Evaluate for malaria.
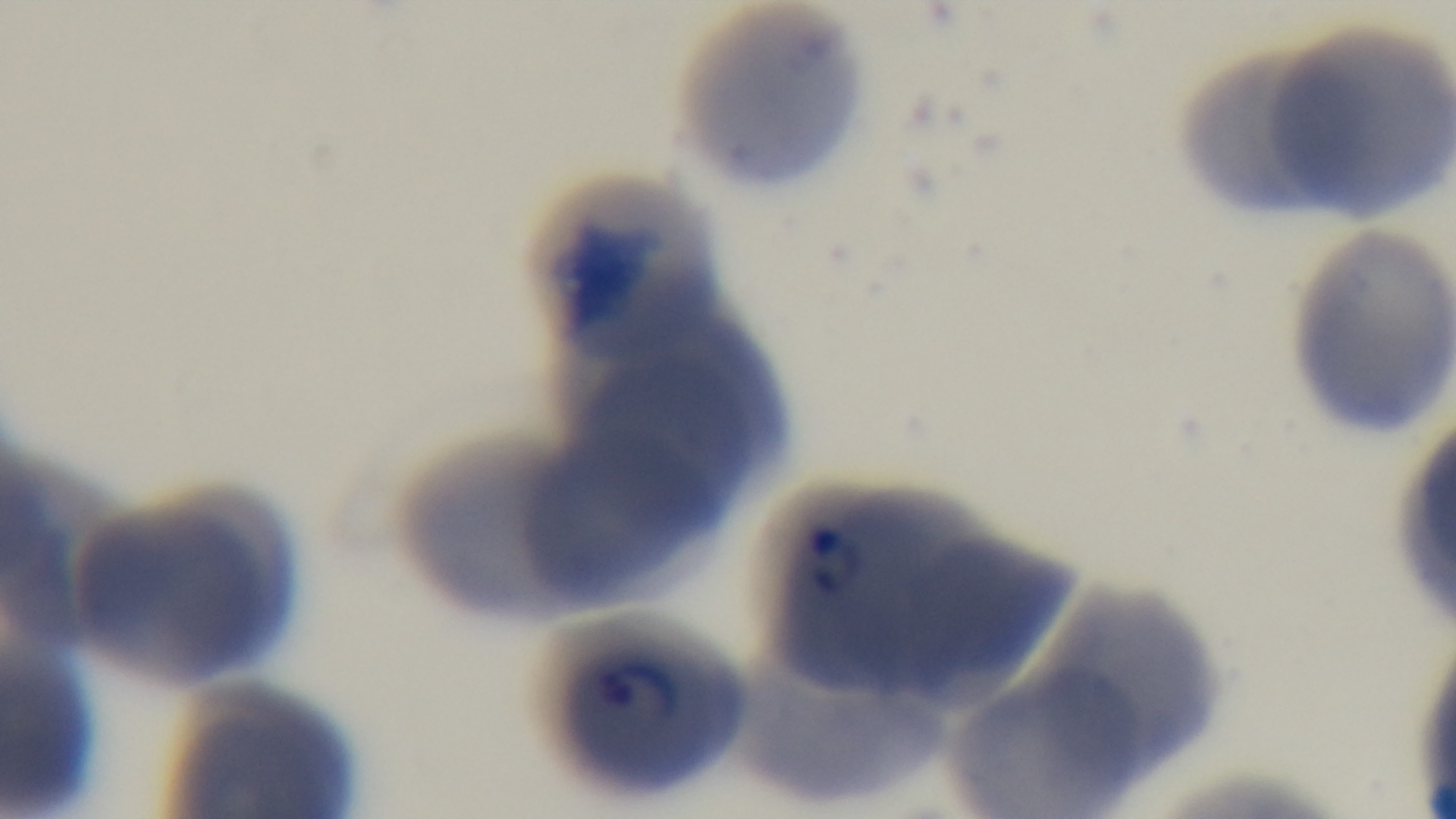
Infected.

Summary:
  - Modality: light microscopy
  - Preparation: thin blood film
  - Stain: Giemsa
  - Objective: 100x oil immersion
  - Field of view: one from the slide
  - Capture: mounted 4K digital camera